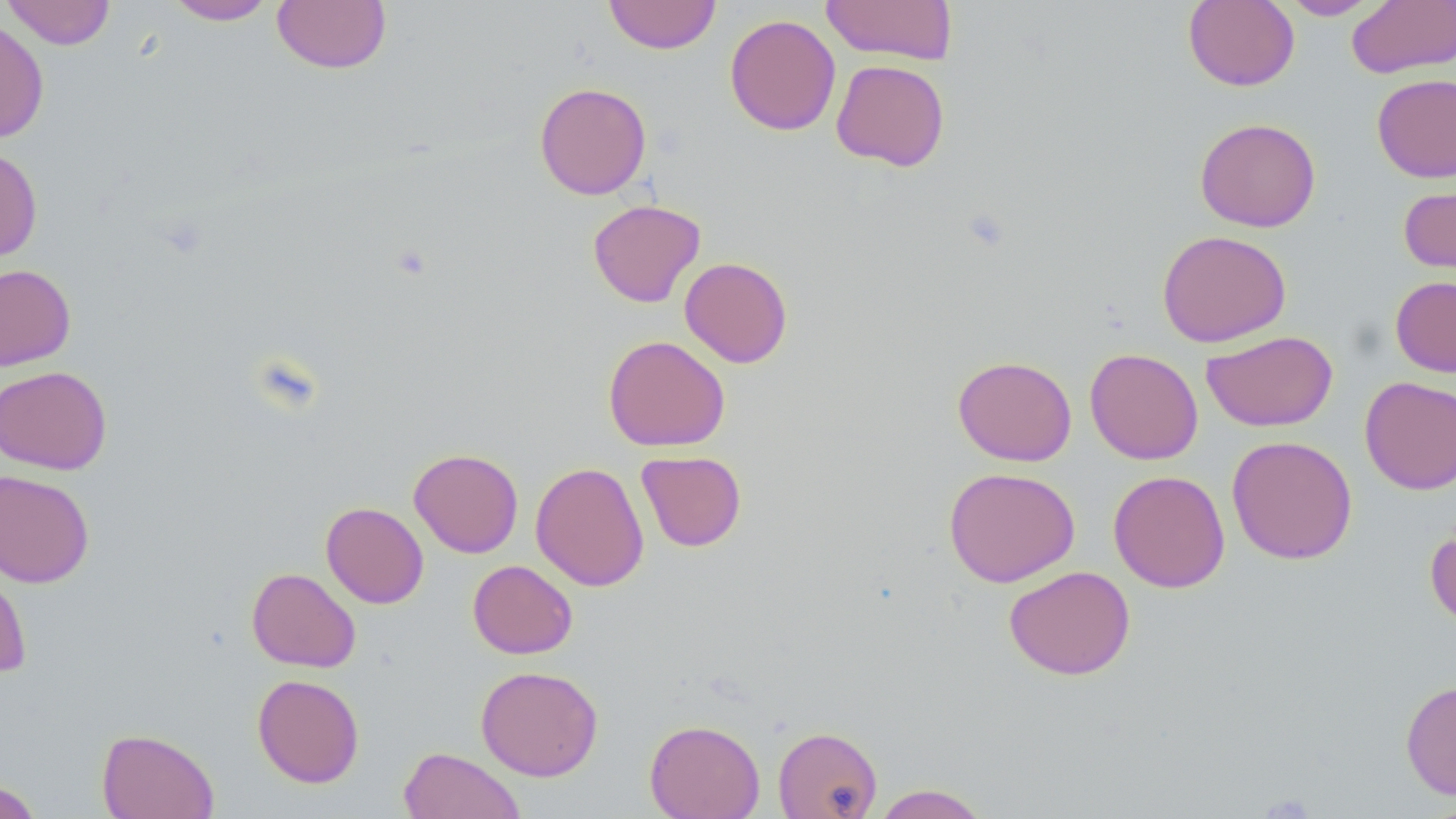
Summary:
  - Coordinate format: approximate bounding boxes as (x1, y1, x2, y2) in pixels
  - Uninfected red blood cell locations: (2, 0, 118, 50), (165, 0, 277, 25), (604, 0, 721, 54), (820, 0, 958, 65), (1183, 0, 1300, 91), (1279, 0, 1384, 20), (272, 1, 392, 74), (1347, 1, 1456, 78), (724, 14, 841, 135), (0, 17, 50, 143), (830, 59, 950, 171), (1371, 73, 1456, 183), (534, 82, 651, 199), (1195, 117, 1321, 232), (0, 147, 42, 261), (1398, 182, 1456, 279), (588, 199, 706, 307), (1157, 230, 1291, 347), (679, 257, 793, 368), (0, 263, 76, 371), (1390, 275, 1456, 377), (1201, 330, 1338, 432), (603, 335, 730, 452), (1084, 348, 1203, 464), (952, 355, 1077, 466), (0, 366, 112, 474), (1360, 376, 1456, 495), (1226, 435, 1358, 564), (409, 448, 523, 558), (636, 451, 747, 552), (530, 462, 649, 591), (942, 466, 1080, 587), (0, 469, 95, 588), (1108, 469, 1231, 593), (321, 502, 429, 608), (1425, 522, 1456, 631), (0, 553, 33, 680), (467, 560, 578, 659), (1004, 565, 1136, 680), (246, 567, 361, 672), (476, 665, 604, 781), (252, 673, 365, 788), (1401, 679, 1456, 800), (644, 719, 764, 818), (773, 726, 882, 819), (96, 728, 219, 819), (398, 746, 525, 819), (0, 779, 44, 819), (871, 784, 991, 818)
  - Slide-level diagnosis: no evidence of blood parasites
  - Modality: light microscopy
  - Preparation: thin blood smear
  - Stain: May-Grünwald-Giemsa
  - Field of view: one of a larger specimen
  - Image size: 1456×819 pixels
  - Magnification: 1000x